Assess the morphology of the erythrocytes.
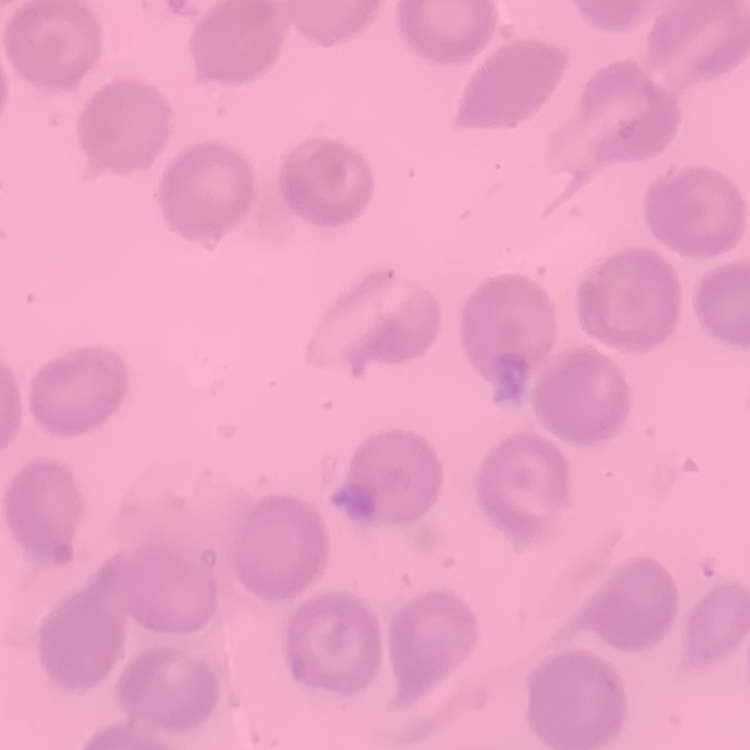
No rouleaux formation.

stain = Field's or Giemsa
preparation = thin blood smear
image type = one tile cut from a larger photomicrograph